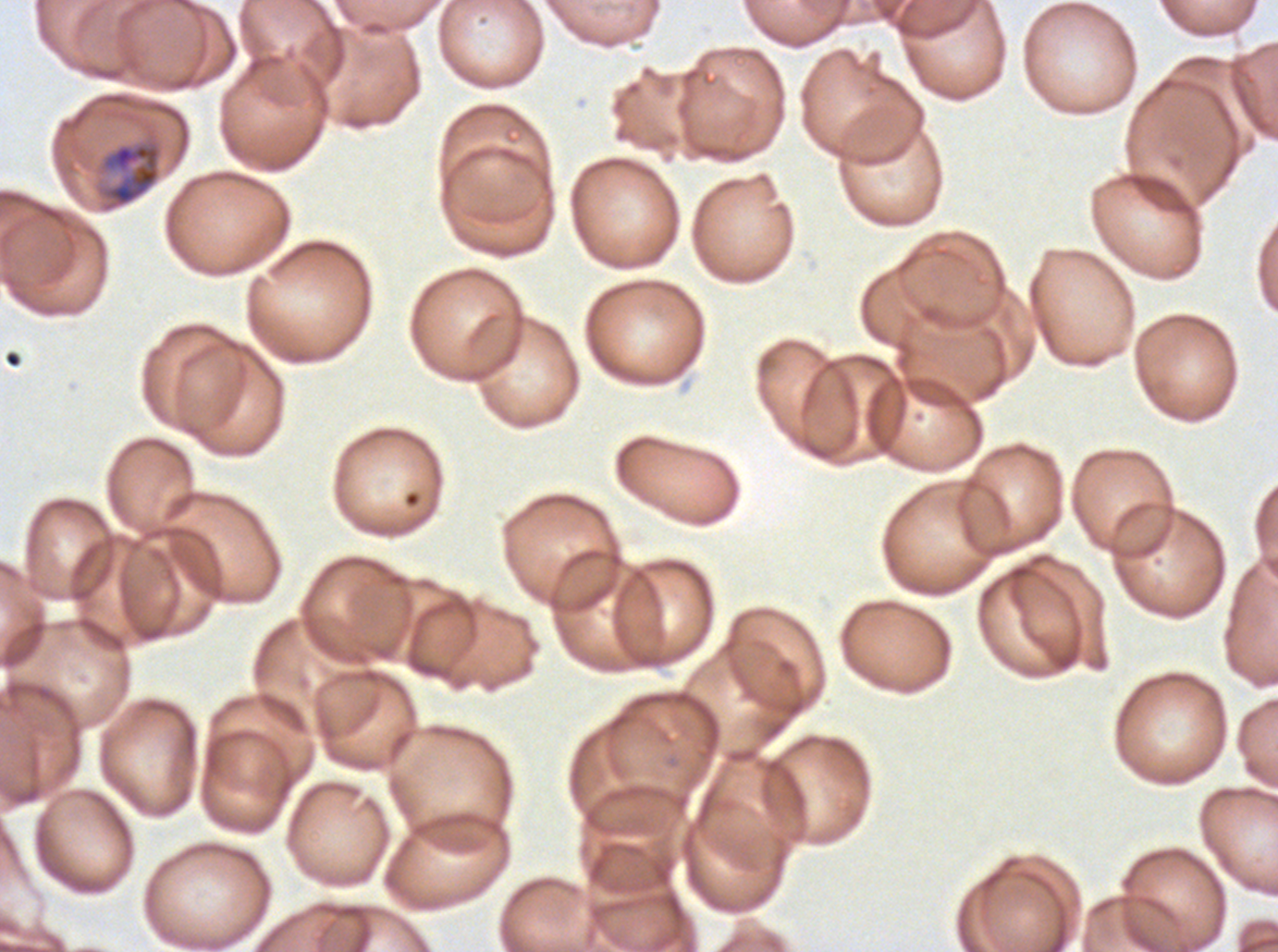
{
  "preparation": "thin blood film",
  "image_size": "1278×952 pixels",
  "stain": "Giemsa",
  "field_of_view": "sub-image separated from a larger composite",
  "specimen": "P. falciparum from a patient in The Gambia, cultured ex vivo for 24 to 48 hours",
  "mid_trophozoite_locations": "approximate bounding rectangles given as corner coordinates in pixels from the top-left: (x1=101, y1=141, x2=162, y2=208)"
}